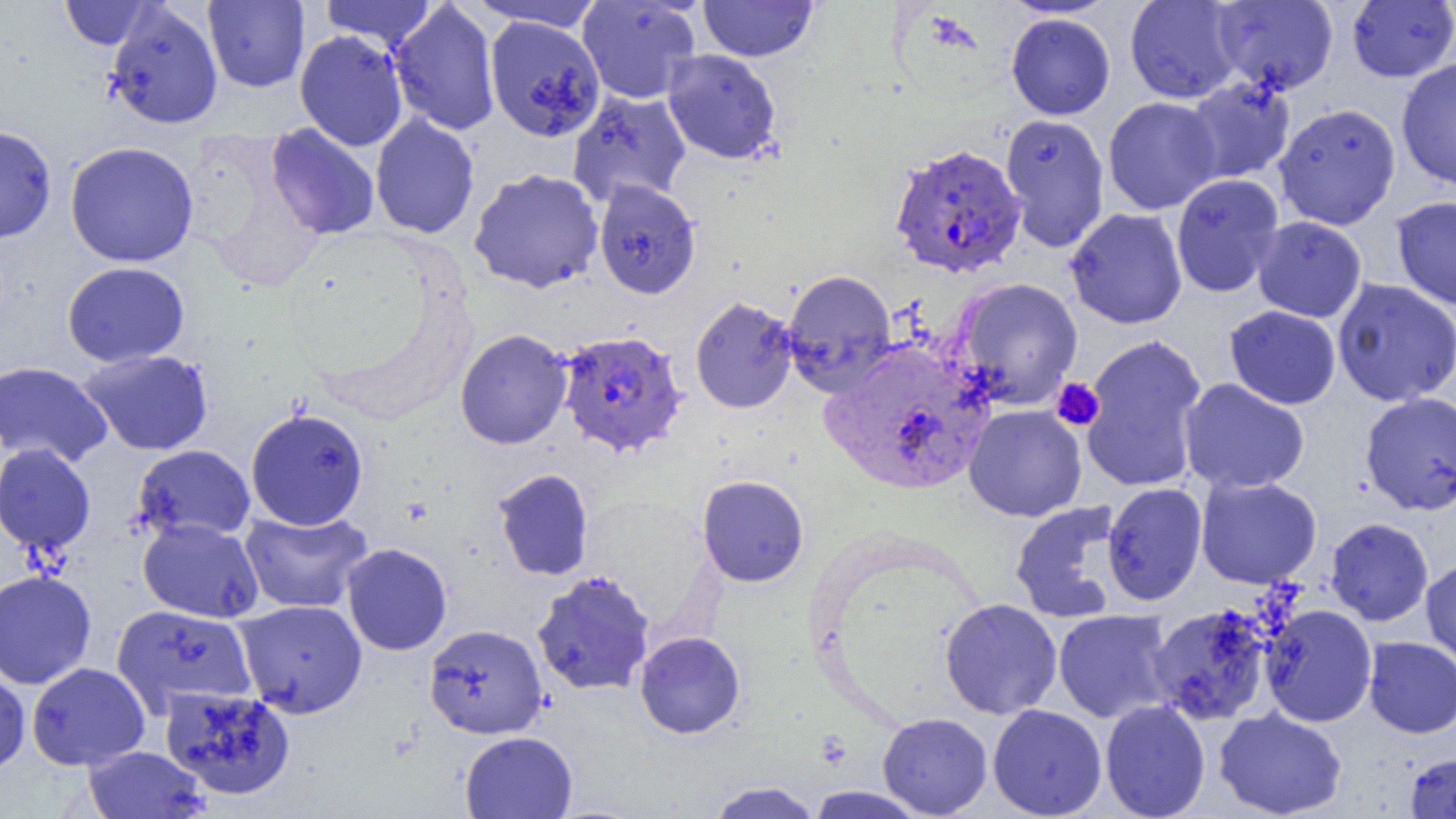
Approximate bounding boxes as (x1,y1)-(x2,y2) corner pairs in pixels. Platelet locations: (1051,378)-(1105,431). Uninfected red blood cell locations: (60,0)-(154,49), (319,0)-(437,50), (471,0)-(605,33), (699,0)-(817,61), (999,0)-(1120,19), (1125,0)-(1245,104), (203,1)-(309,92), (388,1)-(501,137), (577,1)-(701,104), (1211,1)-(1339,95), (1346,1)-(1456,82), (105,2)-(223,130), (1006,13)-(1115,120), (484,15)-(606,142), (294,30)-(408,151), (662,48)-(782,164), (1396,57)-(1456,190), (1183,77)-(1295,184), (567,89)-(692,207), (1103,96)-(1221,215), (1274,103)-(1401,230), (370,113)-(479,239), (999,113)-(1110,252), (0,124)-(57,243), (266,124)-(380,240), (64,141)-(199,267), (468,168)-(604,293), (1170,173)-(1284,298), (593,178)-(701,299), (1392,195)-(1456,310), (1065,207)-(1188,329), (1252,216)-(1367,323), (62,261)-(189,367), (782,269)-(898,394), (952,277)-(1084,409), (1332,278)-(1456,406), (690,296)-(798,414), (1224,305)-(1341,409), (455,329)-(572,450), (1079,334)-(1208,493), (79,349)-(214,455), (0,361)-(112,468), (1178,378)-(1309,494), (1359,391)-(1456,516), (963,404)-(1087,522), (245,407)-(368,530), (0,443)-(96,554), (132,444)-(255,544), (492,468)-(594,581), (697,475)-(809,587), (1196,476)-(1322,589), (1102,482)-(1207,606), (1009,500)-(1125,624), (240,508)-(373,614), (1326,517)-(1433,626), (138,518)-(263,623), (341,543)-(452,656), (1420,555)-(1456,671), (532,569)-(655,696), (0,570)-(97,689), (939,598)-(1062,719), (234,599)-(367,717), (1147,604)-(1274,726), (1261,604)-(1378,727), (112,605)-(257,716), (1053,610)-(1175,723), (423,624)-(548,739), (634,631)-(745,738), (1363,636)-(1456,738), (27,662)-(150,770), (0,665)-(31,776), (160,685)-(296,801), (1100,699)-(1211,818), (988,704)-(1107,818), (1214,707)-(1347,819), (878,712)-(993,818), (459,731)-(577,819), (83,745)-(210,818), (1404,752)-(1456,818), (705,781)-(822,819), (805,786)-(929,818). Plasmodium falciparum-infected red blood cell locations: (889,142)-(1026,279), (558,329)-(688,457), (815,346)-(1000,494). Slide-level diagnosis: Plasmodium falciparum. Optical microscopy. Single field of view. Image is 1456×819 pixels. Thin blood film. 1000x magnification.